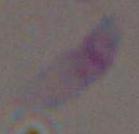

Summary:
  - Magnification: 1000x
  - Modality: micrograph
  - Identification: Toxoplasma gondii